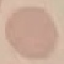
result = negative for malaria parasites
stain = Giemsa
preparation = thin blood film
image type = automatically extracted cell patch, resized to 64 × 64 pixels
capture = smartphone camera at the microscope eyepiece